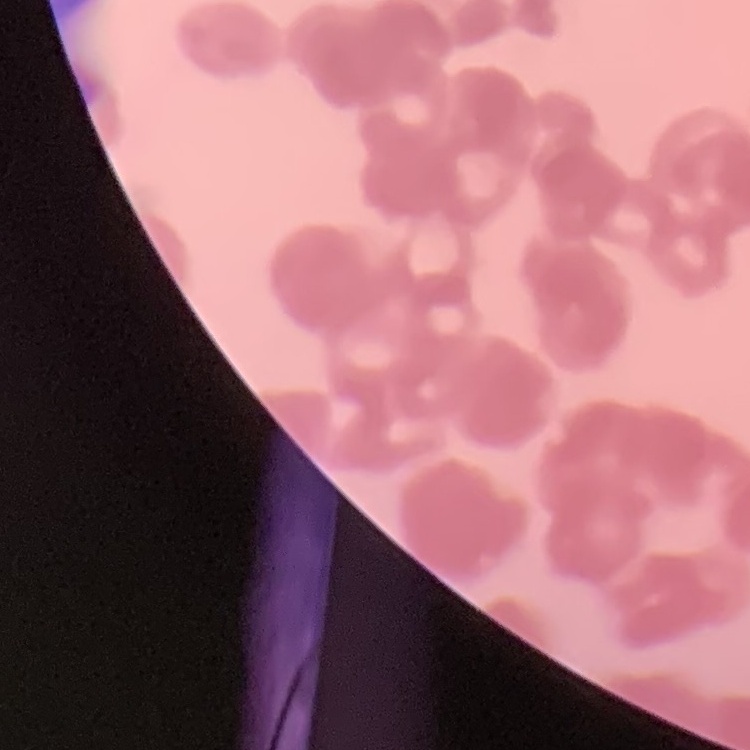

Summary:
  - Red blood cell morphology: rouleaux formation
  - Stain: Field's or Giemsa
  - Image type: one tile cut from a larger photomicrograph
  - Preparation: thin blood film